Assess this cell for malaria.
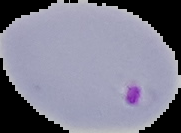
Parasitized.

The area outside the segmented cell region is set to black. Image is 181×133 pixels. From a thin blood film.